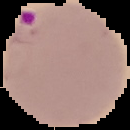
Summary:
  - Image type: segmented cell region on a black background
  - Image size: 130×130 pixels
  - Preparation: thin blood smear
  - Malaria status: parasitized